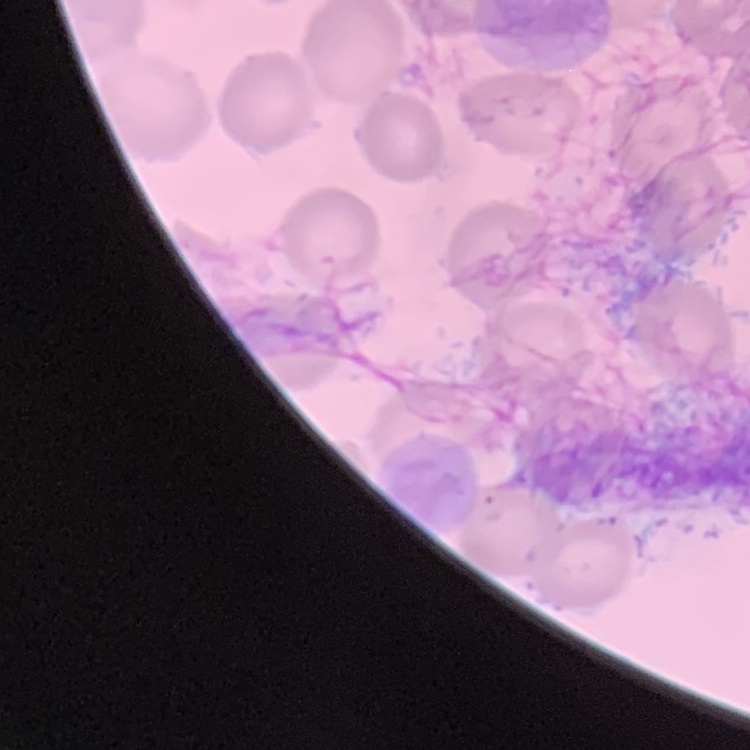
erythrocyte morphology = no rouleaux formation
image type = square crop of a larger photomicrograph
stain = Field's or Giemsa
preparation = thin peripheral smear